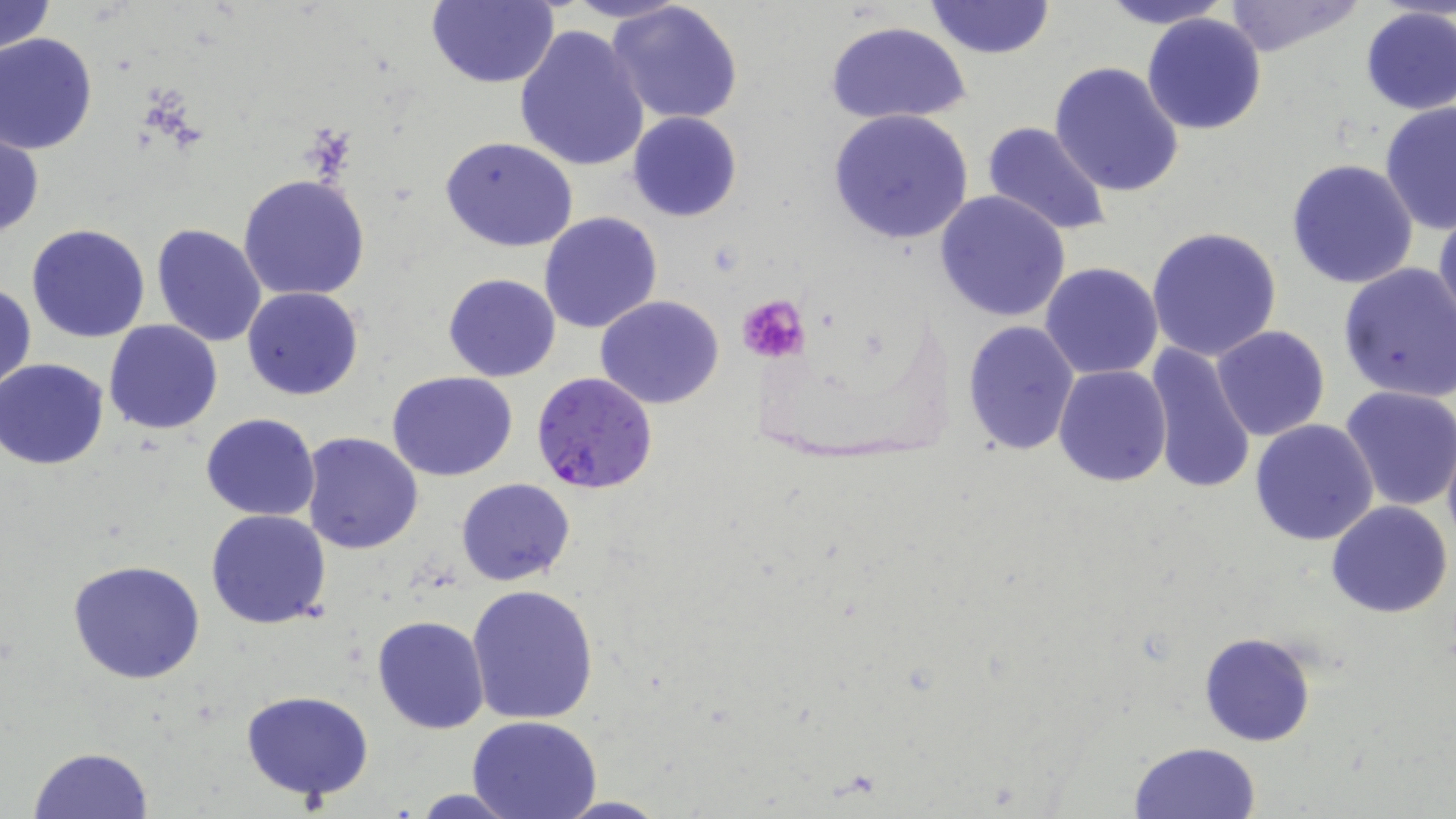
Approximate bounding boxes as (x1,y1)-(x2,y2) corner pairs in pixels. Uninfected red blood cell locations: (0,0)-(56,54), (424,0)-(560,89), (561,0)-(688,25), (1099,0)-(1235,28), (607,1)-(744,127), (924,1)-(1055,61), (1220,1)-(1365,58), (1357,6)-(1455,115), (1141,12)-(1269,135), (825,22)-(971,126), (514,23)-(650,173), (0,32)-(99,153), (1048,61)-(1185,197), (1379,101)-(1456,235), (827,109)-(975,247), (627,111)-(743,222), (981,122)-(1113,238), (1,128)-(43,241), (440,136)-(581,253), (1285,157)-(1419,288), (237,173)-(371,302), (934,189)-(1073,323), (1433,206)-(1455,335), (538,211)-(664,333), (26,223)-(151,343), (151,224)-(268,348), (1145,226)-(1282,362), (1337,262)-(1456,402), (1040,263)-(1164,381), (442,272)-(560,382), (0,282)-(36,397), (242,286)-(364,400), (596,295)-(725,408), (960,320)-(1081,456), (103,321)-(224,435), (1211,326)-(1329,442), (1141,342)-(1256,496), (1,359)-(112,468), (1052,364)-(1172,488), (387,370)-(517,482), (1340,384)-(1456,512), (202,413)-(320,521), (1248,417)-(1379,547), (299,432)-(423,555), (1443,434)-(1456,557), (456,478)-(576,586), (1327,501)-(1453,620), (206,510)-(331,629), (68,560)-(206,685), (467,584)-(600,725), (372,615)-(490,734), (1200,633)-(1317,747), (242,690)-(374,801), (468,715)-(602,819), (1129,741)-(1262,818), (27,747)-(154,819), (408,787)-(526,819), (551,796)-(671,817). Plasmodium falciparum-infected red blood cell locations: (531,373)-(658,494). Platelet locations: (735,295)-(811,364). Slide-level diagnosis: Plasmodium falciparum. Captured at 1000x magnification. Light microscopy. Thin blood smear. One field of a larger specimen. May-Grünwald-Giemsa-stained preparation. Image is 1456×819 pixels.